Classify this cell by malaria status.
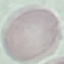
It is uninfected.

image type = cell patch, automatically extracted from a larger field of view and resized to 64 × 64 pixels
stain = Giemsa
preparation = thin blood film
capture = smartphone camera at the microscope eyepiece